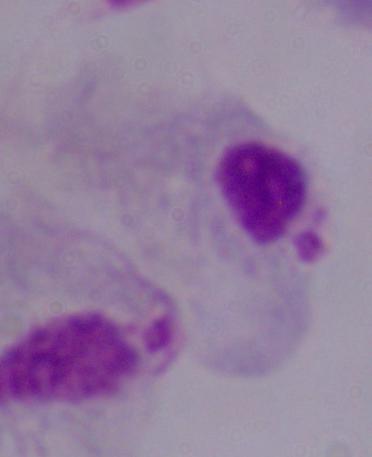
modality: micrograph
identification: trichomonad
magnification: 1000x